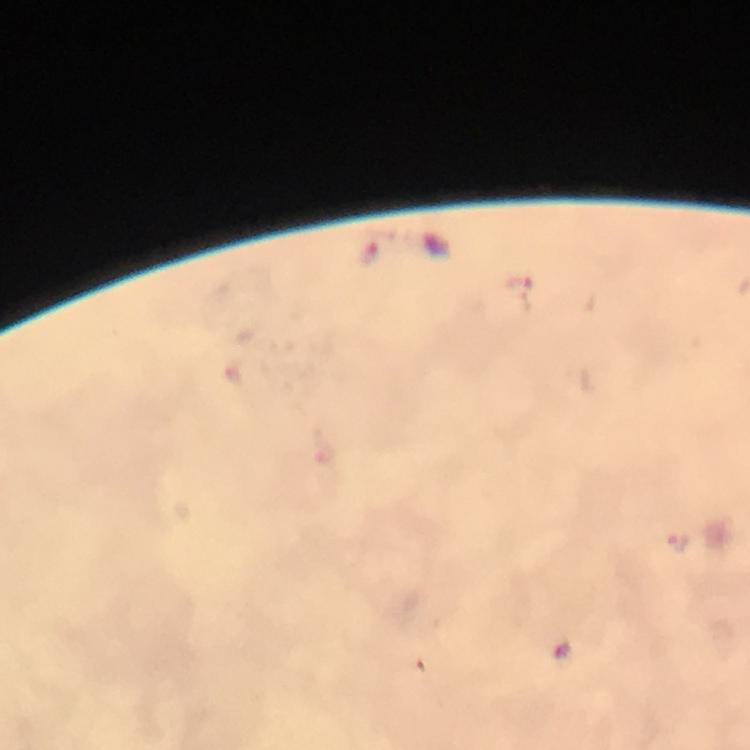

Approximate object centers, in pixels from the top-left corner.
Summary:
  - Plasmodium parasite locations: (x=369, y=256), (x=518, y=284), (x=677, y=543), (x=561, y=651)
  - Stain: Giemsa
  - Preparation: thick smear
  - Immersion oil: used
  - Context: from a diagnostic examination for malaria
  - Cropped from: one field of view
  - Capture: smartphone mounted on the microscope
  - Magnification: 100x
  - Image size: 750×750 pixels